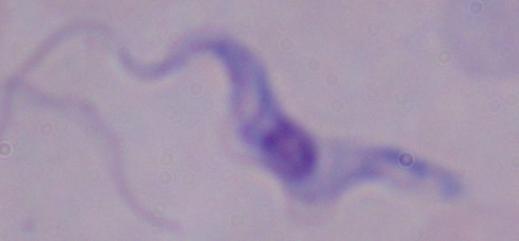

identification = trypanosome
modality = micrograph
magnification = 1000x